Locate every uninfected red blood cell.
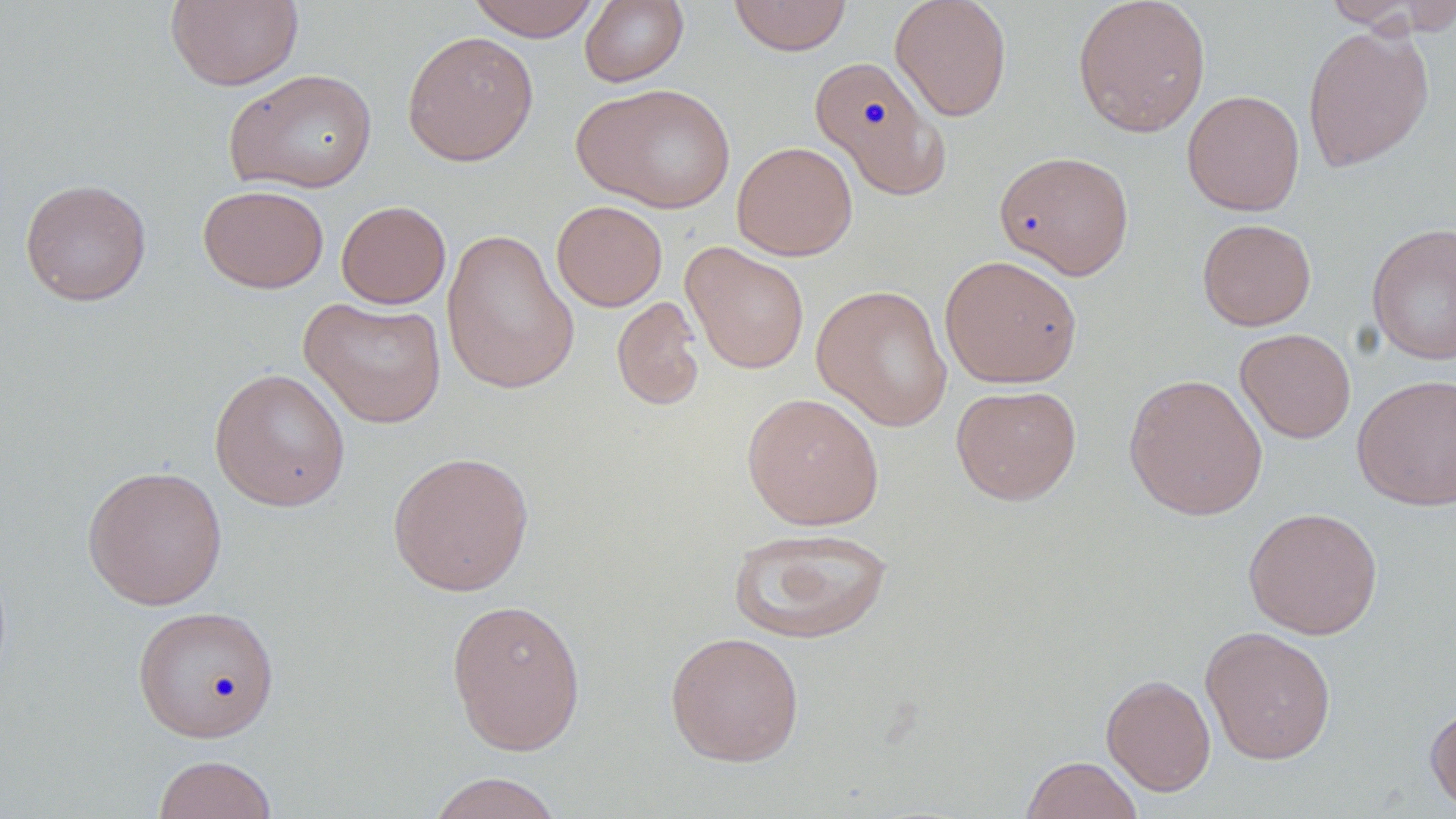
Approximate bounding boxes as named x1/y1/x2/y2 corners in pixels.
Uninfected red blood cells: (x1=165, y1=0, x2=304, y2=92), (x1=466, y1=0, x2=600, y2=41), (x1=579, y1=0, x2=689, y2=87), (x1=728, y1=0, x2=852, y2=56), (x1=889, y1=0, x2=1012, y2=122), (x1=1072, y1=0, x2=1211, y2=137), (x1=1323, y1=0, x2=1452, y2=33), (x1=1302, y1=23, x2=1435, y2=173), (x1=401, y1=30, x2=539, y2=166), (x1=809, y1=56, x2=951, y2=200), (x1=225, y1=68, x2=378, y2=193), (x1=572, y1=82, x2=736, y2=213), (x1=1182, y1=90, x2=1305, y2=216), (x1=732, y1=141, x2=858, y2=261), (x1=993, y1=149, x2=1135, y2=279), (x1=19, y1=178, x2=151, y2=306), (x1=197, y1=184, x2=330, y2=293), (x1=336, y1=200, x2=451, y2=309), (x1=551, y1=200, x2=668, y2=311), (x1=1197, y1=218, x2=1316, y2=331), (x1=1366, y1=222, x2=1456, y2=365), (x1=441, y1=227, x2=580, y2=396), (x1=681, y1=242, x2=810, y2=374), (x1=940, y1=255, x2=1082, y2=388), (x1=811, y1=283, x2=952, y2=431), (x1=299, y1=296, x2=447, y2=429), (x1=612, y1=296, x2=705, y2=411), (x1=1235, y1=328, x2=1356, y2=443), (x1=209, y1=368, x2=350, y2=511), (x1=1123, y1=373, x2=1268, y2=521), (x1=1351, y1=373, x2=1456, y2=511), (x1=951, y1=384, x2=1082, y2=505), (x1=741, y1=392, x2=885, y2=530), (x1=387, y1=450, x2=535, y2=596), (x1=82, y1=465, x2=228, y2=610), (x1=1243, y1=506, x2=1383, y2=639), (x1=729, y1=527, x2=893, y2=644), (x1=446, y1=596, x2=586, y2=757), (x1=131, y1=605, x2=281, y2=742), (x1=1199, y1=625, x2=1337, y2=765), (x1=665, y1=630, x2=805, y2=767), (x1=1101, y1=673, x2=1216, y2=796), (x1=1425, y1=701, x2=1456, y2=814), (x1=153, y1=754, x2=278, y2=819), (x1=1020, y1=755, x2=1144, y2=818), (x1=426, y1=771, x2=565, y2=819).

Slide-level diagnosis: no evidence of blood parasites. Optical microscopy. Single field of view. May-Grünwald-Giemsa stain. Thin blood film. 1000x magnification. Image is 1456×819 pixels.